Give the position of every Plasmodium parasite.
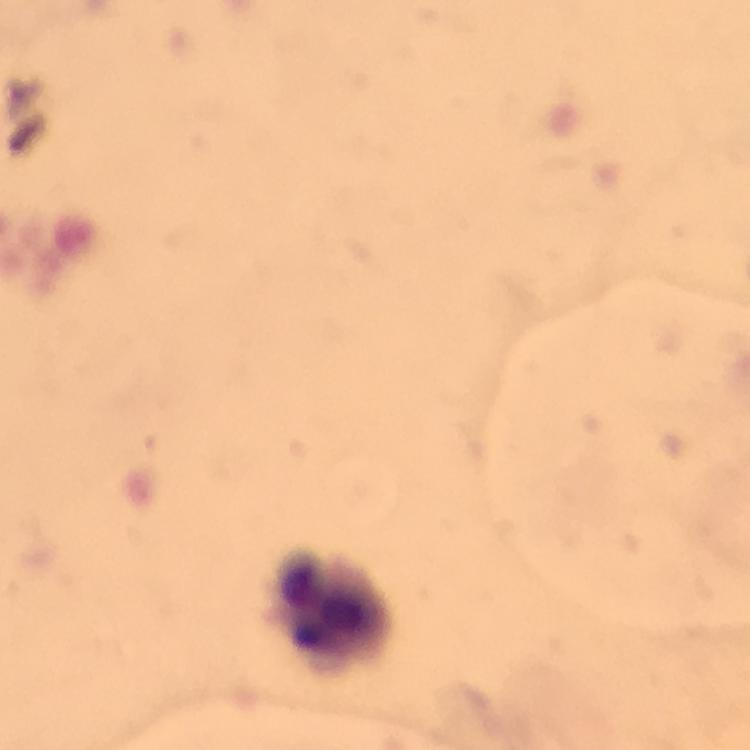
No Plasmodium parasites seen.

Approximate centers as {x, y} in pixels. Leukocyte locations: {333, 611}. Cropped region of a single field of view. Thick blood film. Photographed with a smartphone mounted on the microscope. Image is 750×750 pixels. From a diagnostic examination for malaria. At 100x magnification. Giemsa-stained preparation. Immersion oil applied.